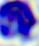 Captured at 400x magnification. Photomicrograph. A white blood cell is shown.